Name the cell type shown.
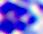
This is a leukocyte.

Photomicrograph. Captured at 400x magnification.